Assess this cell for malaria.
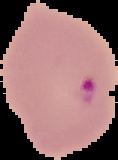

Parasitized.

image size = 118×160 pixels
image type = cell region segmented out of the field of view; surrounding area masked to black
preparation = thin blood film